State which parasite is depicted.
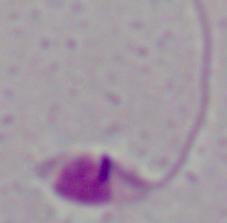
Leishmania.

magnification = 1000x
modality = micrograph